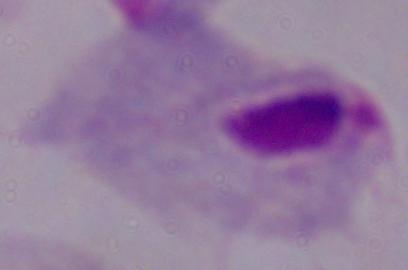
modality = photomicrograph
identification = trichomonad
magnification = 1000x